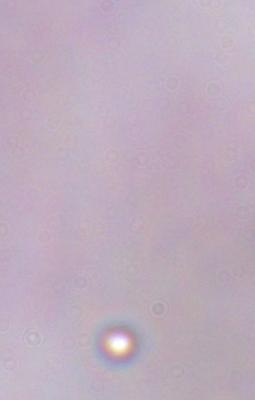

magnification: 1000x
modality: micrograph
identification: trypanosome